Give the extent of all Plasmodium falciparum-infected red blood cells.
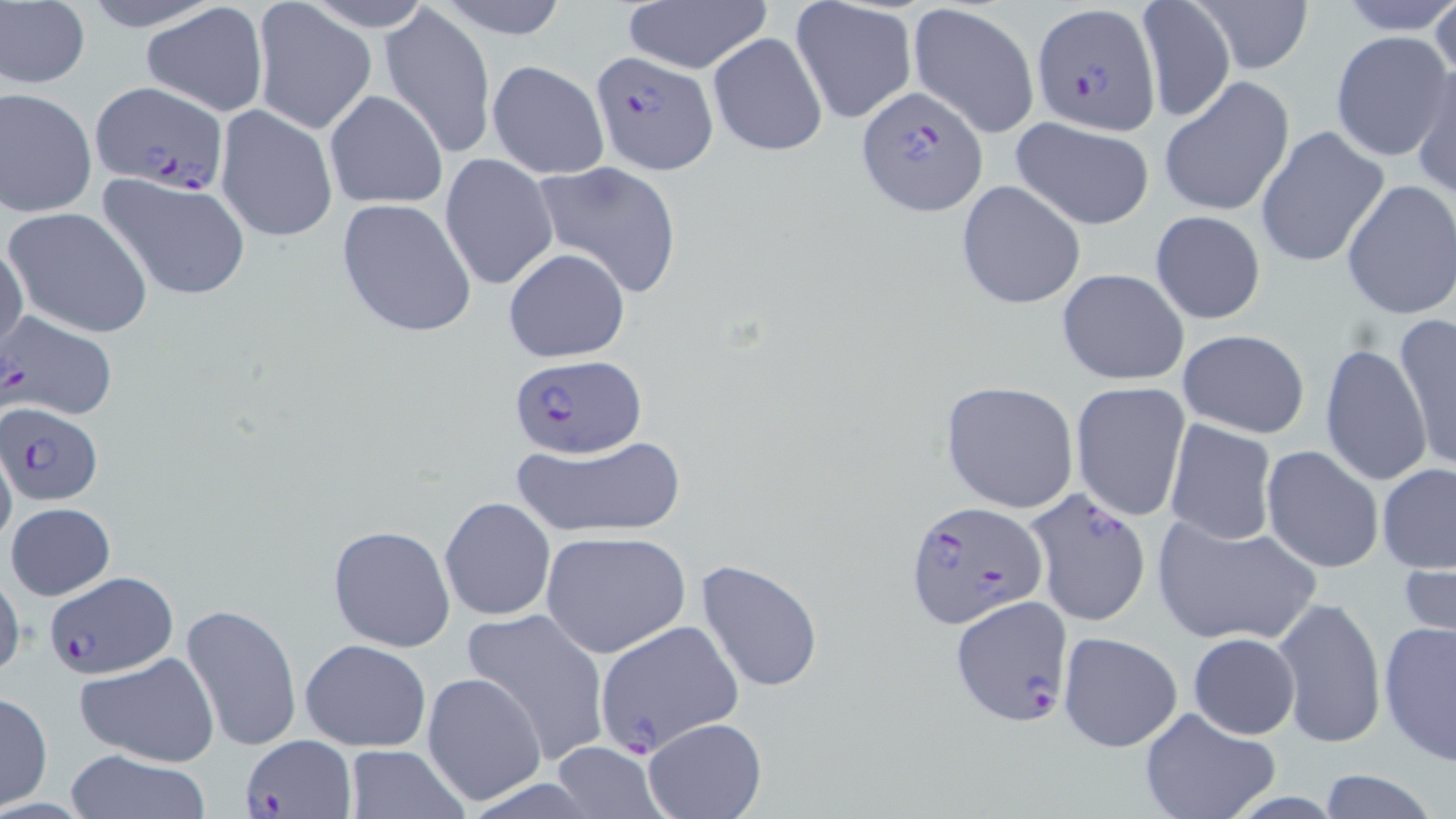
Approximate bounding boxes as (x1,y1)-(x2,y2) corner pairs in pixels.
Plasmodium falciparum-infected red blood cells: (1032,4)-(1161,136), (590,48)-(718,177), (88,82)-(228,196), (855,85)-(989,214), (1,311)-(117,421), (508,354)-(643,454), (2,402)-(104,508), (1025,488)-(1154,626), (904,499)-(1049,631), (42,568)-(177,681), (953,596)-(1073,724), (240,736)-(355,819).

Summary:
  - Uninfected red blood cell locations: (74,0)-(230,32), (306,0)-(433,31), (431,0)-(571,39), (620,0)-(772,75), (1191,0)-(1314,74), (1429,0)-(1456,89), (1,1)-(91,90), (791,1)-(918,125), (906,1)-(1041,139), (1136,1)-(1235,123), (140,2)-(270,118), (250,2)-(373,133), (379,5)-(495,158), (1329,30)-(1450,162), (707,32)-(827,158), (488,60)-(609,179), (1411,61)-(1455,200), (1159,75)-(1296,217), (1,87)-(98,218), (324,90)-(448,209), (215,105)-(338,242), (1011,119)-(1155,230), (1254,124)-(1390,270), (441,153)-(558,291), (529,161)-(684,297), (98,171)-(251,302), (1341,179)-(1456,320), (956,181)-(1086,310), (334,197)-(479,338), (4,206)-(154,339), (1149,209)-(1267,325), (0,238)-(27,360), (503,248)-(630,362), (1056,268)-(1190,385), (1394,314)-(1455,472), (1176,329)-(1311,440), (1320,342)-(1432,488), (939,380)-(1080,513), (1069,380)-(1190,524), (1164,418)-(1277,544), (510,435)-(688,538), (0,436)-(16,556), (1259,445)-(1384,575), (1378,463)-(1456,574), (441,497)-(555,620), (5,503)-(115,602), (1151,512)-(1320,647), (326,525)-(456,651), (539,530)-(690,658), (1399,552)-(1456,658), (694,559)-(825,694), (0,566)-(25,689), (1270,596)-(1387,748), (180,601)-(302,753), (462,606)-(611,766), (591,619)-(743,759), (1378,620)-(1456,764), (1057,631)-(1184,753), (1187,632)-(1300,740), (301,639)-(432,752), (76,651)-(222,768), (421,671)-(546,808), (0,691)-(52,810), (1137,706)-(1281,819), (642,718)-(765,819), (343,745)-(470,818), (545,745)-(669,819), (62,749)-(214,819), (1314,768)-(1443,819)
  - Slide-level diagnosis: Plasmodium falciparum
  - Preparation: thin blood film
  - Modality: light microscopy
  - Magnification: 1000x
  - Image size: 1456×819 pixels
  - Field of view: single
  - Stain: May-Grünwald-Giemsa